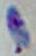
Summary:
  - Magnification: 1000x
  - Modality: micrograph
  - Identification: Toxoplasma gondii